Give the extent of all Plasmodium malariae-infected red blood cells.
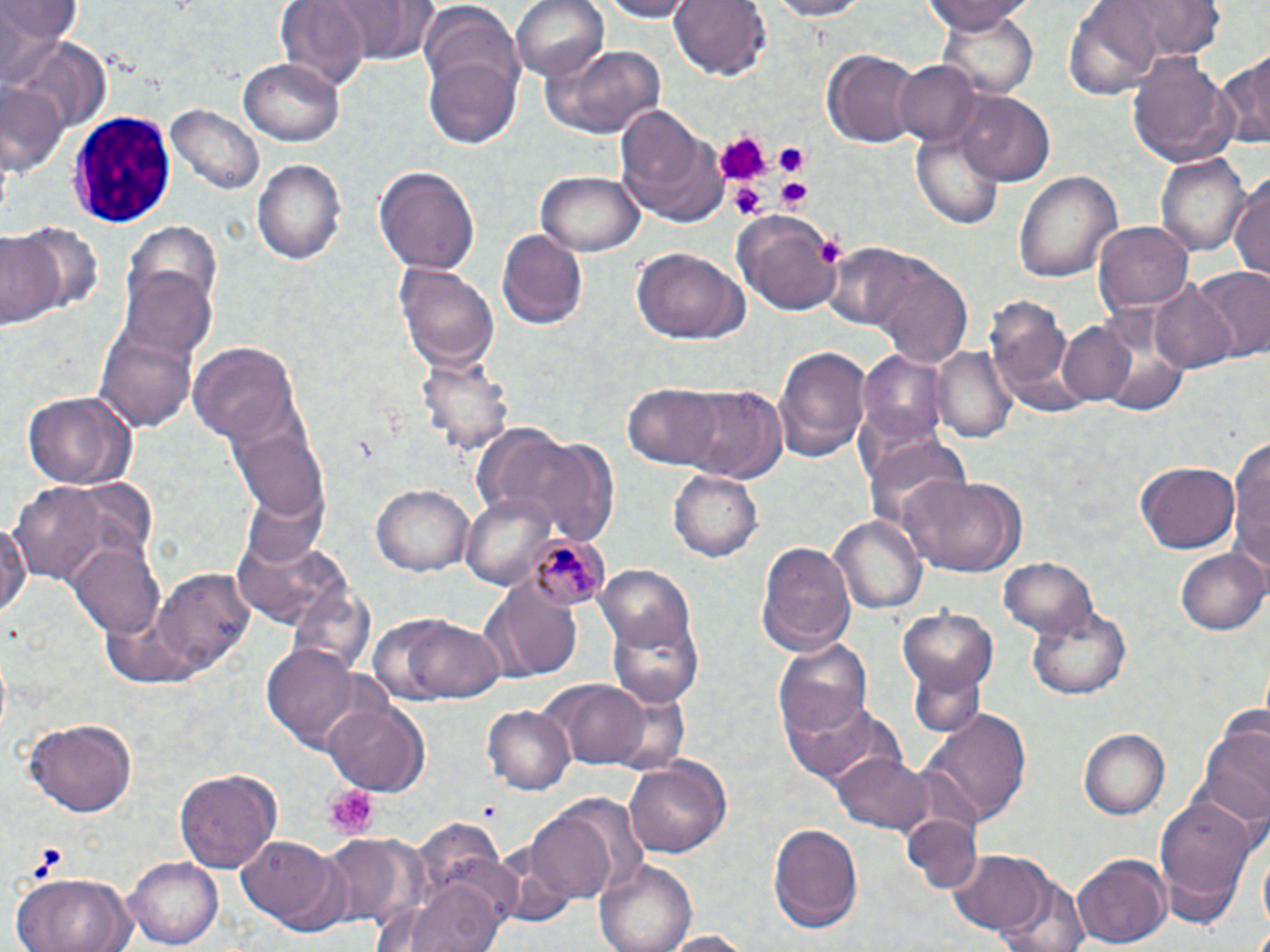
Approximate bounding boxes as (x1,y1)-(x2,y2) corner pairs in pixels.
Plasmodium malariae-infected red blood cells: (529,534)-(614,610).

slide-level diagnosis = Plasmodium malariae
field of view = single
platelet locations = approximate bounding boxes as (x1,y1)-(x2,y2) corner pairs in pixels: (715,131)-(765,184), (774,143)-(808,177), (774,177)-(811,212), (732,181)-(765,218), (817,236)-(845,269), (325,786)-(378,838)
image size = 1270×952 pixels
magnification = 1000x
stain = May-Grünwald-Giemsa
uninfected red blood cell locations = approximate bounding boxes as (x1,y1)-(x2,y2) corner pairs in pixels: (272,0)-(374,92), (512,0)-(611,82), (591,0)-(699,21), (667,0)-(770,82), (759,0)-(875,20), (919,0)-(1036,33), (1112,0)-(1230,58), (1065,1)-(1166,98), (0,4)-(80,55), (420,8)-(522,105), (939,11)-(1038,98), (545,43)-(669,138), (1219,47)-(1270,154), (820,49)-(921,148), (1126,51)-(1239,169), (425,54)-(520,150), (239,58)-(343,147), (895,61)-(982,147), (0,86)-(67,180), (959,92)-(1056,187), (611,101)-(728,227), (166,103)-(263,196), (910,122)-(1005,230), (1156,152)-(1249,258), (253,157)-(345,264), (373,164)-(480,273), (536,169)-(645,256), (1016,169)-(1123,283), (1228,173)-(1270,286), (734,208)-(842,317), (1094,221)-(1194,313), (494,224)-(588,329), (0,230)-(63,330), (630,247)-(747,345), (864,256)-(973,367), (394,262)-(500,372), (119,265)-(218,363), (1189,266)-(1270,362), (1151,281)-(1240,374), (984,298)-(1078,412), (1058,321)-(1137,405), (100,334)-(197,430), (191,344)-(299,446), (773,344)-(869,463), (932,344)-(1018,445), (859,349)-(953,442), (414,360)-(512,469), (673,382)-(788,483), (621,383)-(728,470), (19,388)-(137,489), (235,426)-(329,521), (1231,432)-(1270,577), (526,438)-(620,543), (865,445)-(972,523), (1136,461)-(1239,553), (672,468)-(764,560), (900,472)-(1025,578), (6,480)-(125,585), (372,482)-(474,576), (460,490)-(546,591), (0,514)-(33,624), (831,515)-(926,616), (232,534)-(354,630), (758,539)-(856,656), (70,542)-(165,637), (1177,547)-(1270,636), (997,556)-(1100,640), (594,565)-(697,659), (148,569)-(255,675), (483,579)-(584,682), (898,605)-(998,698), (1027,605)-(1132,700), (368,609)-(509,707), (609,610)-(703,708), (773,640)-(874,742), (264,644)-(363,747), (545,678)-(653,768), (780,693)-(905,788), (324,700)-(426,793), (482,704)-(576,794), (923,712)-(1029,829), (24,717)-(138,818), (1197,724)-(1270,826), (1079,729)-(1168,819), (833,750)-(933,833), (621,755)-(731,859), (172,766)-(281,873), (1156,795)-(1258,907), (527,797)-(640,905), (902,816)-(983,894), (767,821)-(867,935), (237,833)-(340,930), (321,834)-(413,929), (949,850)-(1055,941), (1071,854)-(1169,950), (126,855)-(224,947), (594,858)-(697,952), (12,870)-(137,951), (991,871)-(1092,952), (394,876)-(510,952), (651,930)-(761,950)
preparation = thin blood smear
modality = light microscopy
white blood cell locations = approximate bounding boxes as (x1,y1)-(x2,y2) corner pairs in pixels: (69,112)-(177,230)